Outline each Plasmodium vivax-infected red blood cell.
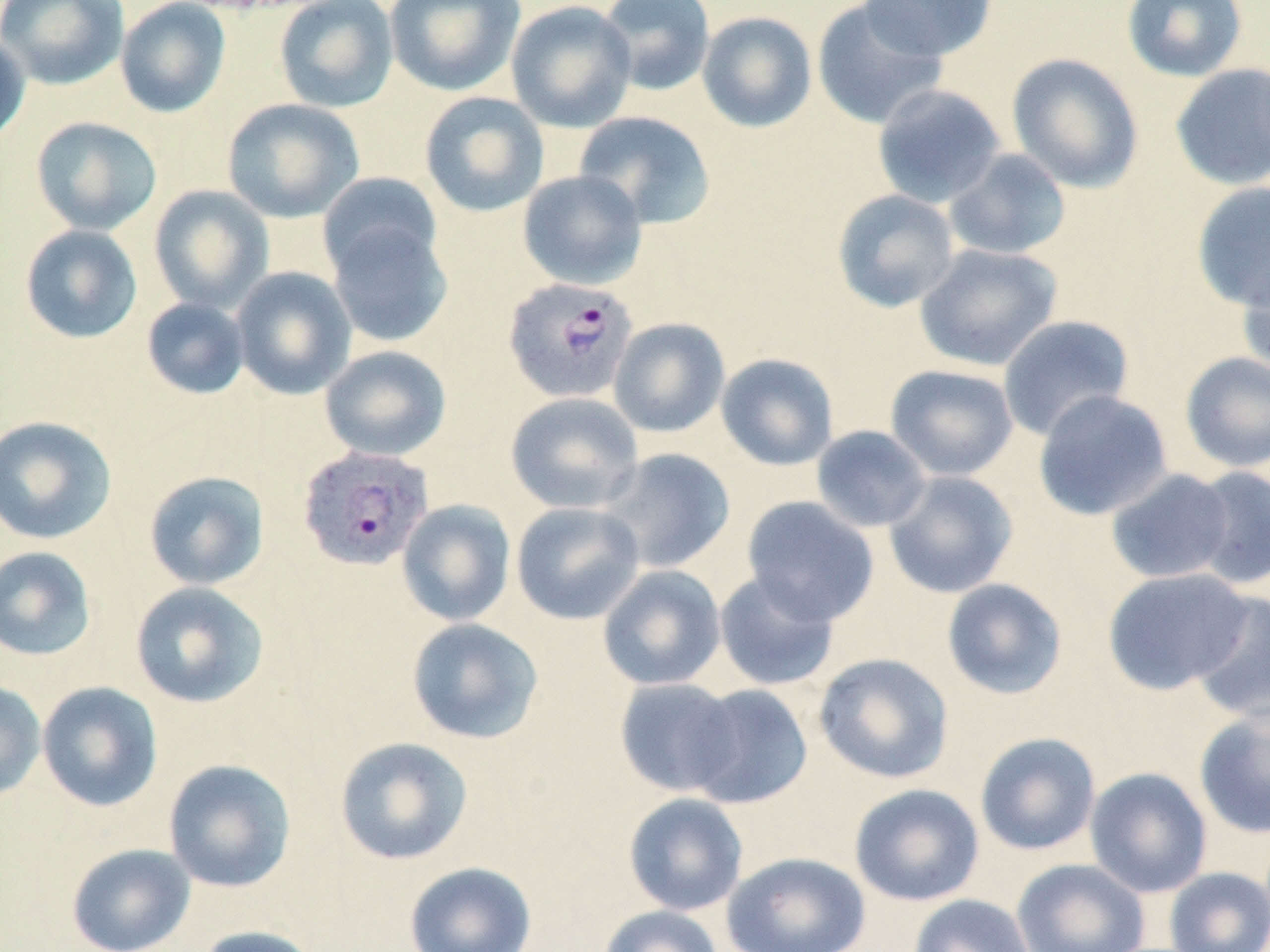

Approximate bounding boxes as (x1,y1)-(x2,y2) corner pairs in pixels.
Plasmodium vivax-infected red blood cells: (503,278)-(638,403), (297,445)-(434,571).

Uninfected red blood cell locations: (0,0)-(129,90), (115,0)-(231,118), (274,0)-(399,113), (385,0)-(525,96), (597,0)-(716,96), (859,0)-(997,60), (1121,0)-(1248,82), (506,1)-(637,132), (811,1)-(949,130), (697,11)-(817,133), (0,30)-(31,148), (1006,53)-(1144,193), (1169,62)-(1270,191), (872,84)-(1006,208), (419,92)-(550,217), (222,98)-(365,223), (574,111)-(716,229), (30,116)-(163,235), (943,148)-(1072,261), (517,170)-(647,290), (317,172)-(443,280), (1191,181)-(1270,313), (148,185)-(274,313), (831,189)-(960,313), (325,217)-(453,347), (19,224)-(143,344), (914,243)-(1063,371), (1236,260)-(1270,380), (231,267)-(356,400), (141,297)-(250,400), (998,314)-(1135,441), (608,317)-(730,438), (319,345)-(452,461), (1179,351)-(1270,473), (715,353)-(839,471), (885,364)-(1019,481), (1032,389)-(1173,521), (505,392)-(644,514), (0,415)-(117,545), (811,425)-(932,532), (599,448)-(736,573), (1188,465)-(1270,589), (1105,468)-(1236,584), (144,470)-(269,590), (883,470)-(1018,599), (740,495)-(880,625), (397,499)-(516,626), (510,501)-(645,625), (0,546)-(97,661), (597,565)-(726,690), (1101,567)-(1255,695), (714,570)-(840,691), (941,578)-(1068,700), (129,581)-(269,709), (1188,589)-(1270,727), (406,617)-(544,744), (813,652)-(955,784), (615,677)-(742,797), (0,680)-(46,801), (37,681)-(163,812), (684,684)-(813,809), (1194,708)-(1270,839), (975,732)-(1101,856), (333,736)-(474,865), (163,758)-(297,893), (1085,767)-(1212,898), (849,783)-(985,906), (623,792)-(748,916), (66,843)-(196,952), (721,851)-(871,952), (1011,858)-(1150,952), (404,861)-(537,952), (1163,866)-(1270,952), (908,894)-(1036,952), (598,905)-(724,952), (194,925)-(319,952). Slide-level diagnosis: Plasmodium vivax. May-Grünwald-Giemsa stain. Image is 1270×952 pixels. 1000x magnification. Light microscopy. Thin blood film. One field of a larger specimen.